Report the malaria status of this cell.
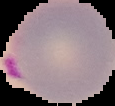

Parasitized.

Summary:
  - Preparation: thin blood smear
  - Image type: segmented cell region with the area outside set to black
  - Image size: 115×106 pixels